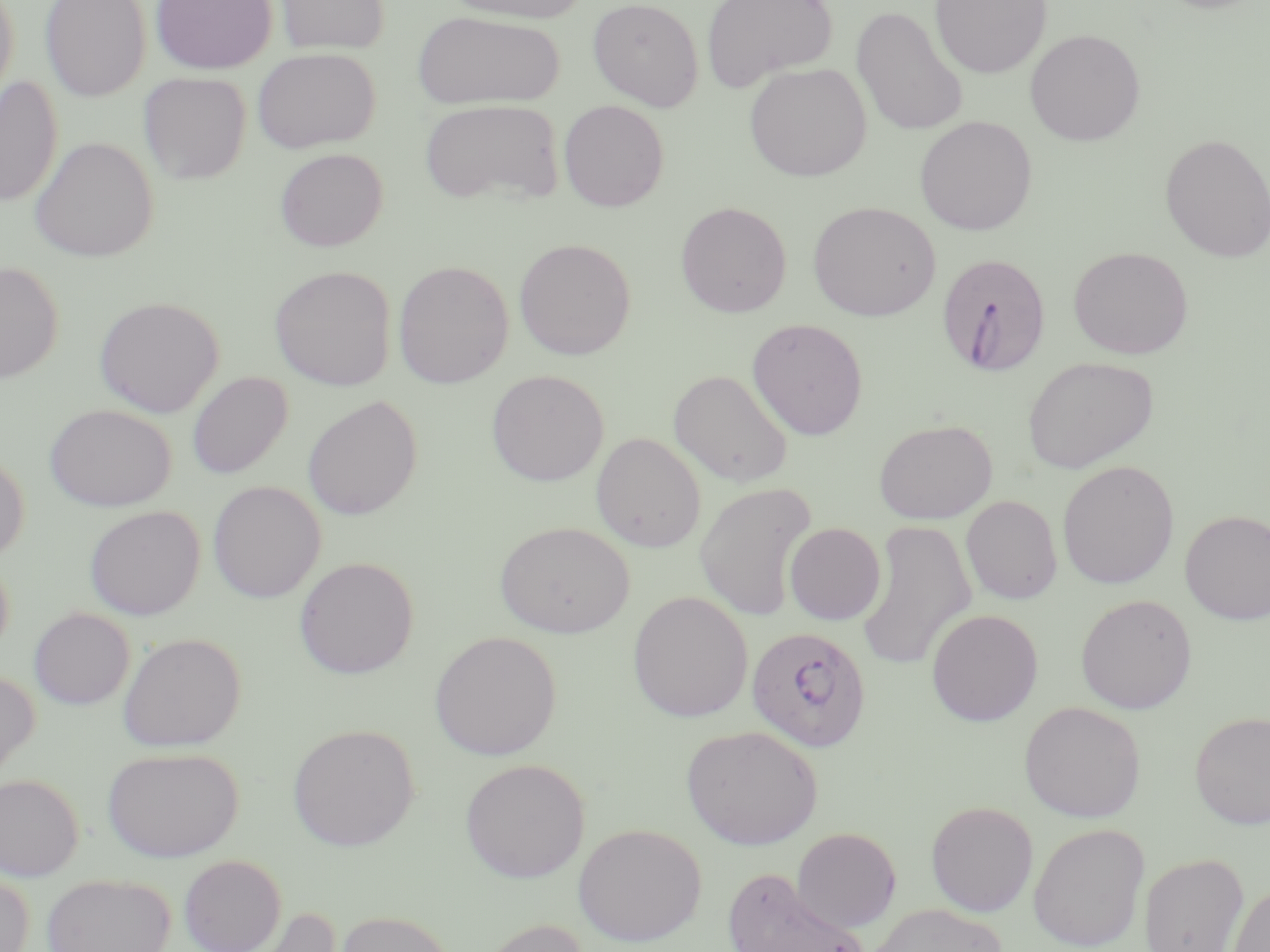

Plasmodium falciparum-infected red blood cell locations = approximate bounding boxes as (x1,y1)-(x2,y2) corner pairs in pixels: (936,252)-(1052,377), (745,626)-(871,753)
slide-level diagnosis = Plasmodium falciparum
preparation = thin blood film
modality = optical microscopy
field of view = one of a larger specimen
image size = 1270×952 pixels
uninfected red blood cell locations = approximate bounding boxes as (x1,y1)-(x2,y2) corner pairs in pixels: (0,0)-(20,110), (40,0)-(151,101), (150,0)-(278,74), (274,0)-(391,56), (443,0)-(591,24), (588,0)-(704,111), (701,0)-(838,93), (929,0)-(1052,79), (1151,0)-(1269,14), (851,5)-(968,136), (413,10)-(564,110), (1025,29)-(1145,146), (252,47)-(379,153), (744,62)-(872,182), (138,72)-(251,185), (0,75)-(63,207), (419,99)-(564,207), (558,100)-(669,212), (915,116)-(1037,235), (1160,133)-(1270,263), (29,136)-(159,262), (273,148)-(388,252), (674,201)-(792,317), (807,201)-(941,321), (514,238)-(636,360), (1068,246)-(1194,359), (393,260)-(513,389), (0,261)-(63,383), (270,265)-(396,391), (94,296)-(225,418), (746,318)-(869,440), (1022,356)-(1159,473), (486,370)-(609,486), (668,370)-(794,487), (187,371)-(293,479), (303,395)-(423,520), (45,404)-(176,512), (874,419)-(998,525), (591,432)-(706,552), (0,450)-(30,564), (1057,460)-(1179,589), (207,480)-(326,604), (694,480)-(816,622), (961,495)-(1062,605), (84,505)-(205,620), (1180,510)-(1270,625), (856,519)-(977,673), (494,521)-(635,638), (784,522)-(886,625), (0,552)-(14,662), (294,556)-(419,679), (627,591)-(753,723), (1076,593)-(1197,714), (29,607)-(133,709), (926,608)-(1043,726), (429,631)-(562,760), (118,632)-(246,752), (0,669)-(40,781), (1019,701)-(1146,822), (1189,711)-(1270,829), (287,723)-(419,852), (680,724)-(823,850), (102,746)-(243,862), (460,758)-(590,882), (0,773)-(84,881), (925,801)-(1038,917), (573,822)-(706,946), (1028,822)-(1149,951), (792,827)-(902,931), (1138,852)-(1249,952), (178,854)-(287,952), (722,866)-(871,952), (0,869)-(34,952), (41,873)-(176,952), (1228,883)-(1270,952), (868,903)-(1008,952), (235,905)-(344,952), (333,910)-(457,952), (475,917)-(591,952)
magnification = 1000x
stain = May-Grünwald-Giemsa